Mark where platelets are.
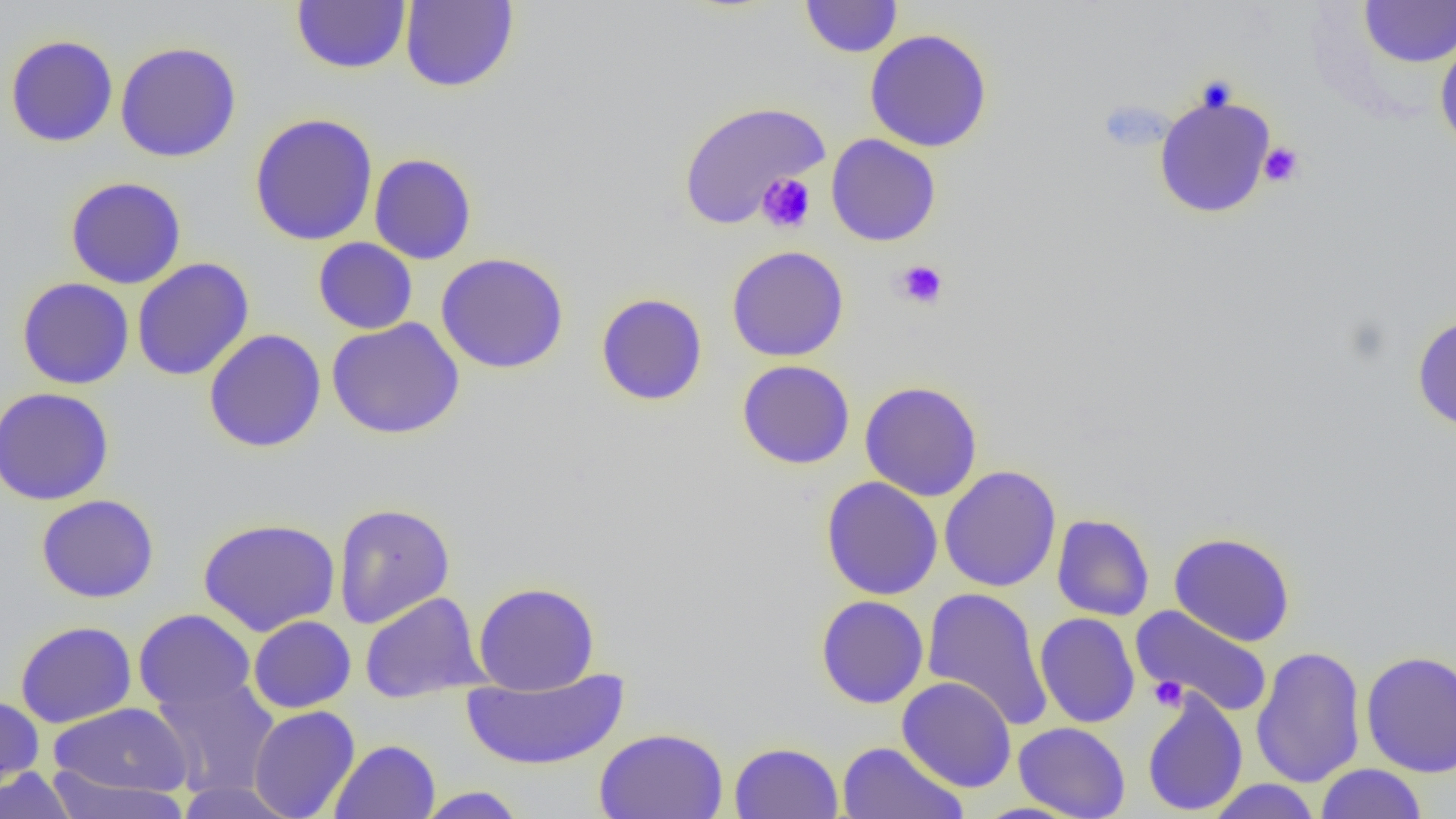
Approximate bounding boxes as (x1,y1)-(x2,y2) corner pairs in pixels.
Platelets: (1258,141)-(1305,188), (756,173)-(816,233), (894,259)-(949,309), (1148,675)-(1188,711).

Summary:
  - Uninfected red blood cell locations: (291,0)-(411,75), (799,0)-(903,58), (400,1)-(519,92), (1359,1)-(1456,68), (864,29)-(994,152), (1434,31)-(1456,156), (5,35)-(119,147), (115,41)-(242,162), (1152,90)-(1277,219), (676,100)-(830,229), (249,113)-(379,247), (825,134)-(941,247), (369,153)-(477,265), (65,176)-(187,289), (313,238)-(418,334), (726,245)-(849,362), (435,252)-(570,374), (132,258)-(254,381), (17,277)-(134,390), (595,292)-(708,407), (1411,312)-(1456,431), (326,318)-(465,439), (203,329)-(326,453), (737,359)-(856,469), (859,380)-(983,501), (0,387)-(114,506), (939,465)-(1062,592), (821,476)-(944,600), (36,494)-(159,603), (333,502)-(456,628), (1052,513)-(1154,621), (198,518)-(340,636), (1169,532)-(1296,647), (473,581)-(600,694), (921,587)-(1053,732), (359,591)-(488,703), (815,594)-(929,709), (1131,604)-(1274,718), (134,608)-(256,713), (1035,612)-(1140,728), (248,615)-(356,713), (15,621)-(137,727), (1250,645)-(1366,788), (1361,650)-(1456,777), (461,667)-(631,771), (151,675)-(281,798), (897,676)-(1017,792), (1141,688)-(1248,817), (0,696)-(44,794), (50,702)-(193,796), (249,705)-(360,819), (1013,722)-(1130,818), (594,727)-(729,819), (329,739)-(440,819), (728,741)-(844,819), (836,741)-(968,819), (1314,763)-(1428,819), (46,767)-(191,819), (0,768)-(78,819), (1206,779)-(1321,819), (174,780)-(301,818), (416,786)-(526,818)
  - Slide-level diagnosis: no evidence of blood parasites
  - Magnification: 1000x
  - Field of view: single
  - Preparation: thin blood film
  - Image size: 1456×819 pixels
  - Modality: optical microscopy